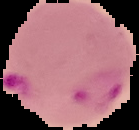

{
  "image_size": "139×130 pixels",
  "preparation": "thin blood smear",
  "image_type": "cell region segmented out of the field of view; surrounding area masked to black",
  "result": "malaria parasites identified"
}